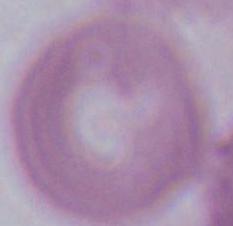 A red blood cell is seen. 1000x magnification. Photomicrograph.